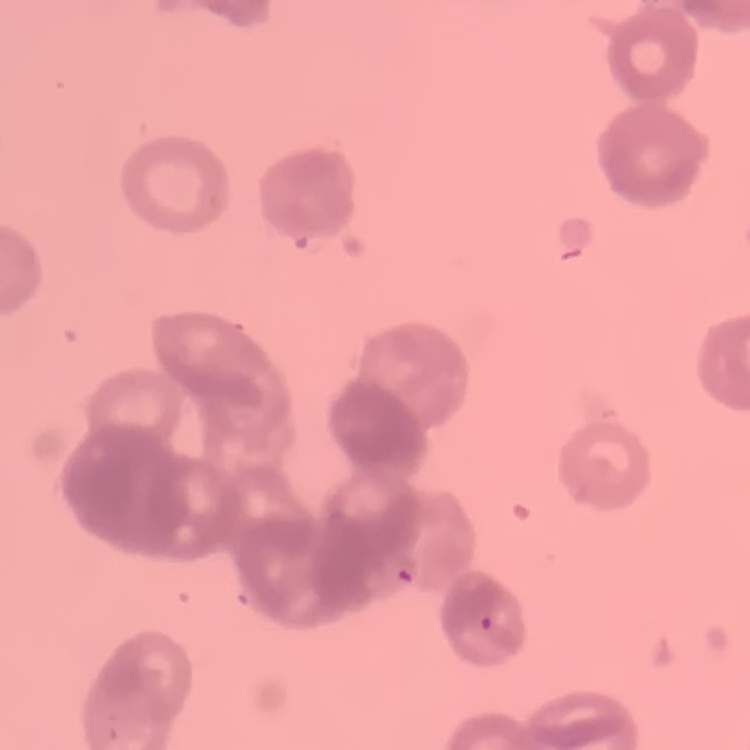

The erythrocytes exhibit rouleaux formation. Thin blood smear. Stained with either Field's or Giemsa. Square crop of a larger photomicrograph.